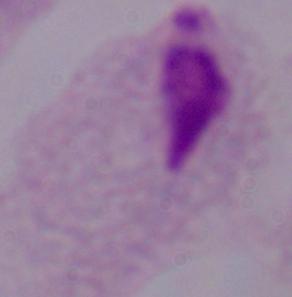

Summary:
  - Identification: trichomonad
  - Magnification: 1000x
  - Modality: micrograph